Assess this cell for malaria.
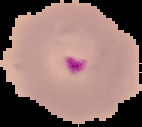
It is parasitized.

image size = 142×127 pixels
preparation = thin blood film
image type = segmented cell region with the area outside set to black